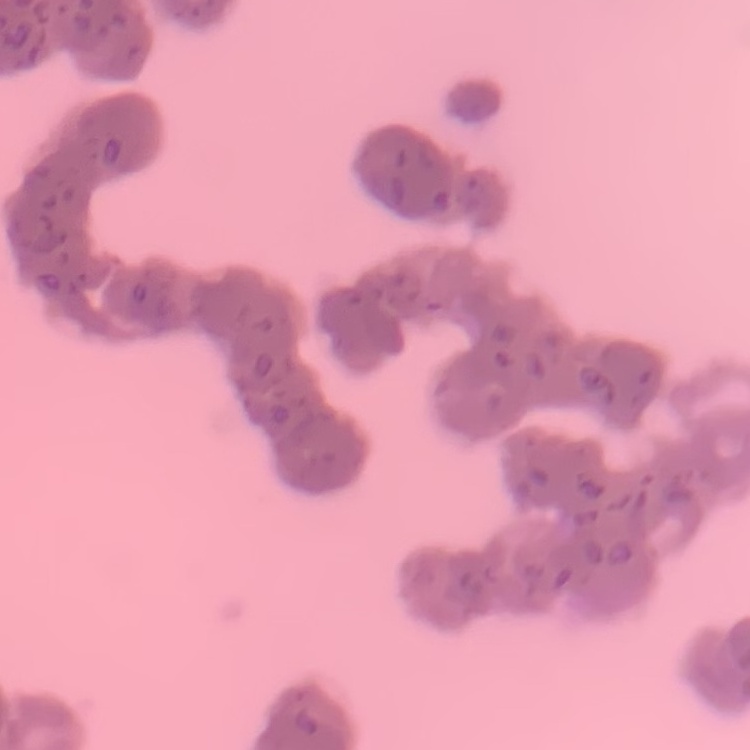 The red blood cells show rouleaux formation. Square crop of a larger photomicrograph. Thin blood film. Stained with either Field's or Giemsa.